Locate every blood parasite and identify its species.
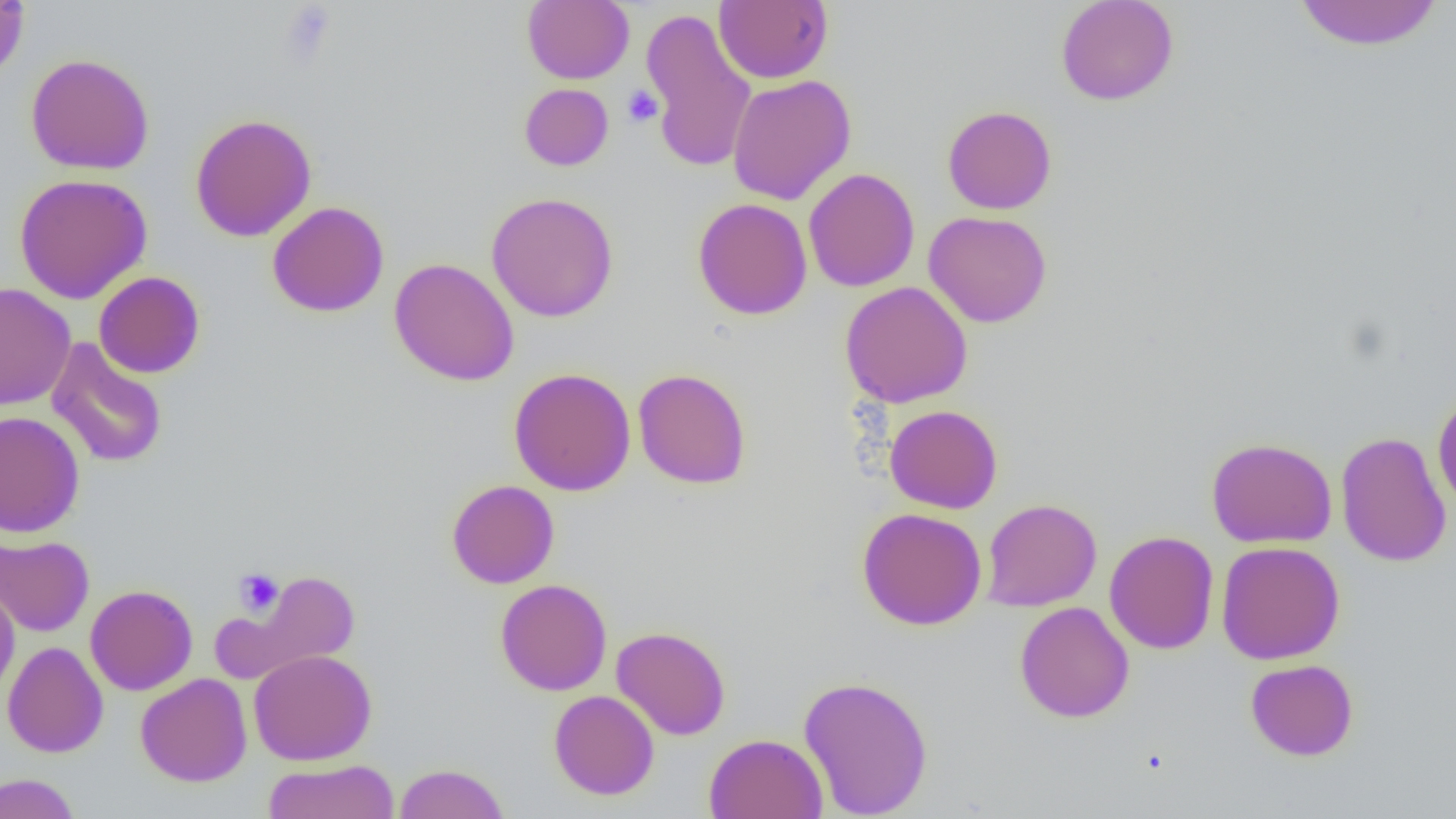
No blood parasites observed.

Approximate bounding boxes as (x1, y1, x2, y2) in pixels. Platelet locations: (278, 2, 338, 66), (622, 86, 663, 127), (233, 567, 283, 616). Uninfected red blood cell locations: (0, 0, 30, 82), (523, 0, 634, 84), (714, 0, 833, 83), (1055, 0, 1180, 106), (1293, 0, 1444, 51), (640, 7, 756, 173), (25, 53, 155, 175), (727, 74, 856, 205), (519, 83, 614, 171), (942, 105, 1057, 214), (190, 113, 316, 242), (804, 167, 920, 292), (13, 173, 153, 304), (486, 192, 619, 322), (693, 198, 812, 320), (267, 201, 389, 317), (923, 211, 1053, 328), (389, 257, 519, 386), (94, 271, 205, 378), (840, 282, 973, 408), (1, 283, 76, 411), (46, 338, 168, 469), (508, 367, 636, 496), (632, 368, 752, 489), (1432, 389, 1456, 515), (884, 405, 1002, 514), (0, 411, 85, 538), (1335, 431, 1451, 568), (1206, 437, 1338, 548), (446, 479, 560, 588), (981, 498, 1102, 611), (857, 507, 987, 630), (1104, 530, 1219, 654), (0, 534, 94, 636), (1215, 540, 1345, 665), (237, 569, 360, 678), (495, 578, 612, 696), (0, 581, 21, 700), (85, 584, 198, 695), (1015, 601, 1134, 723), (611, 626, 731, 740), (2, 641, 109, 758), (248, 649, 377, 765), (1245, 658, 1359, 761), (136, 666, 377, 775), (135, 673, 252, 787), (797, 674, 934, 818), (548, 690, 660, 800), (704, 733, 828, 819), (261, 758, 399, 819), (394, 763, 509, 819), (0, 773, 81, 819). Slide-level diagnosis: no evidence of blood parasites. Image is 1456×819 pixels. Captured at 1000x magnification. Light microscopy. One field of a larger specimen. Thin blood smear.